Name the parasite shown.
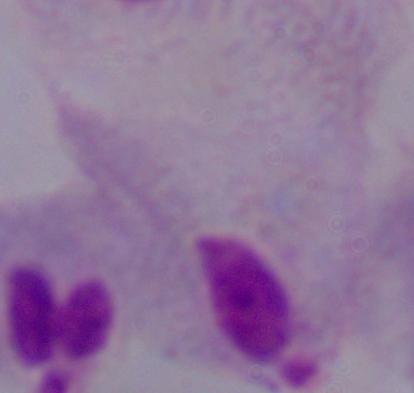

A trichomonad.

Summary:
  - Magnification: 1000x
  - Modality: photomicrograph